Report the malaria status of this cell.
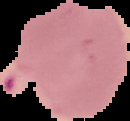
Parasitized.

preparation = thin blood smear
image size = 130×121 pixels
image type = segmented cell region on a black background